Classify this cell by malaria status.
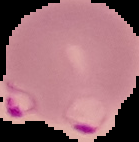

Parasitized.

Segmented cell region on a black background. From a thin blood film. Image is 139×142 pixels.